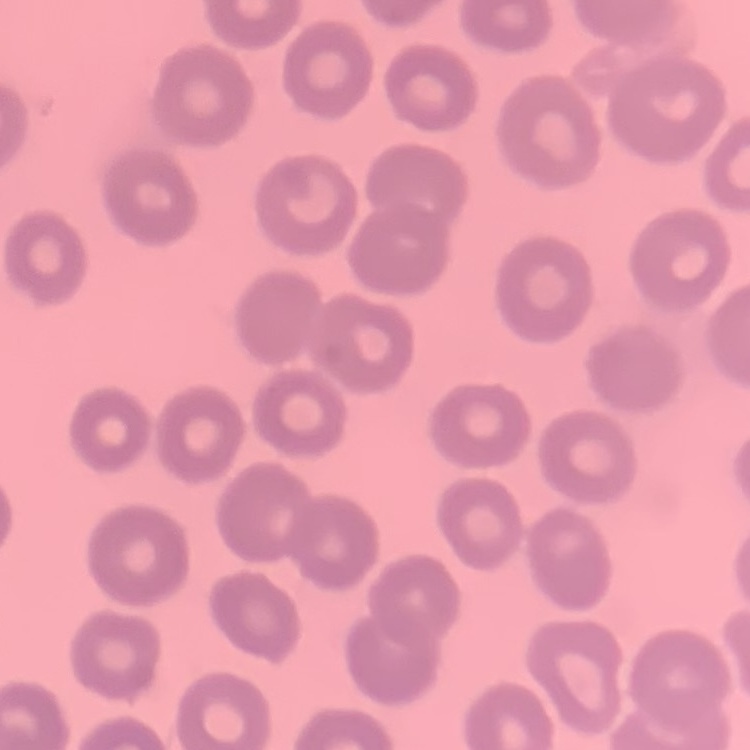

Summary:
  - Red blood cell morphology: no rouleaux formation
  - Stain: Field's or Giemsa
  - Image type: square crop of a larger photomicrograph
  - Preparation: thin blood smear